Locate platelets.
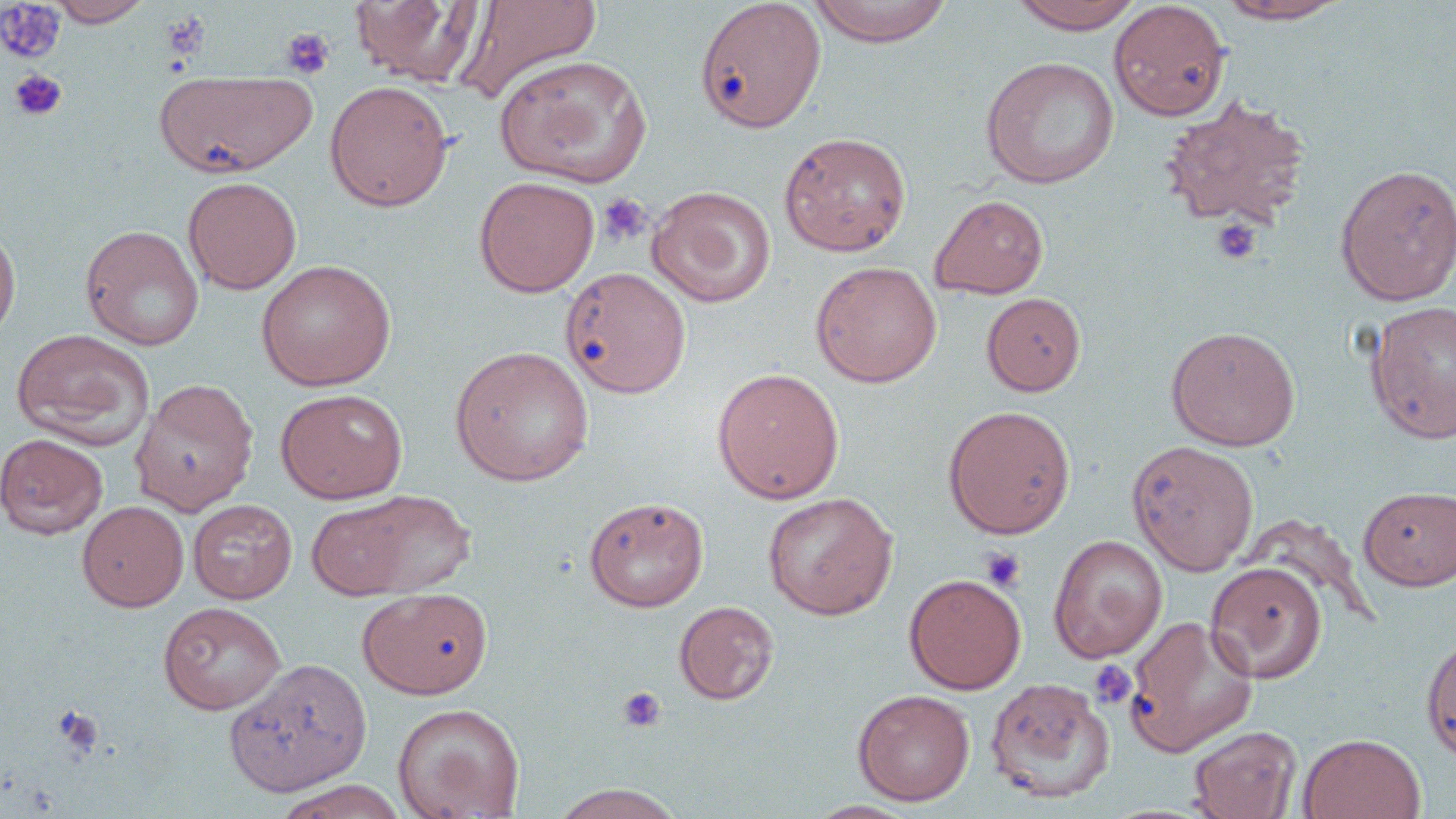

Approximate bounding boxes as (x1, y1, x2, y2) in pixels.
Platelets: (0, 4, 65, 64), (280, 27, 335, 80), (8, 69, 67, 121), (598, 193, 652, 246), (1211, 218, 1263, 265), (979, 546, 1026, 592), (1089, 659, 1137, 709), (617, 686, 666, 733), (52, 704, 104, 760).

Uninfected red blood cell locations: (48, 0, 152, 26), (349, 0, 487, 87), (454, 0, 603, 104), (806, 0, 955, 47), (1006, 0, 1147, 33), (694, 1, 827, 133), (1108, 1, 1231, 121), (1213, 1, 1351, 24), (495, 55, 652, 188), (980, 56, 1120, 189), (155, 69, 315, 177), (324, 80, 453, 212), (1159, 95, 1311, 231), (779, 131, 912, 256), (1334, 163, 1456, 305), (183, 176, 301, 295), (474, 176, 600, 297), (647, 186, 776, 308), (930, 194, 1049, 298), (0, 222, 21, 345), (80, 223, 204, 351), (255, 259, 396, 391), (810, 261, 942, 387), (561, 267, 692, 398), (981, 292, 1086, 396), (1365, 301, 1456, 444), (1165, 325, 1301, 451), (11, 328, 156, 450), (449, 344, 595, 486), (711, 367, 845, 504), (130, 378, 259, 516), (275, 388, 408, 503), (942, 405, 1076, 539), (0, 433, 108, 539), (1126, 440, 1260, 576), (1358, 485, 1456, 591), (334, 489, 477, 597), (762, 492, 898, 620), (584, 496, 709, 612), (306, 498, 417, 600), (187, 499, 297, 604), (77, 500, 188, 611), (1048, 534, 1167, 662), (1205, 561, 1328, 683), (904, 573, 1026, 694), (357, 587, 491, 699), (674, 600, 779, 705), (157, 601, 286, 714), (1123, 615, 1258, 756), (1421, 630, 1456, 764), (224, 658, 372, 797), (984, 677, 1115, 803), (853, 689, 975, 806), (392, 702, 525, 819), (1188, 726, 1303, 819), (1298, 733, 1425, 819), (274, 779, 406, 818), (549, 784, 688, 819). Slide-level diagnosis: negative for blood parasites. One field of a larger specimen. Image is 1456×819 pixels. Thin blood film. May-Grünwald-Giemsa stain. Optical microscopy. 1000x magnification.